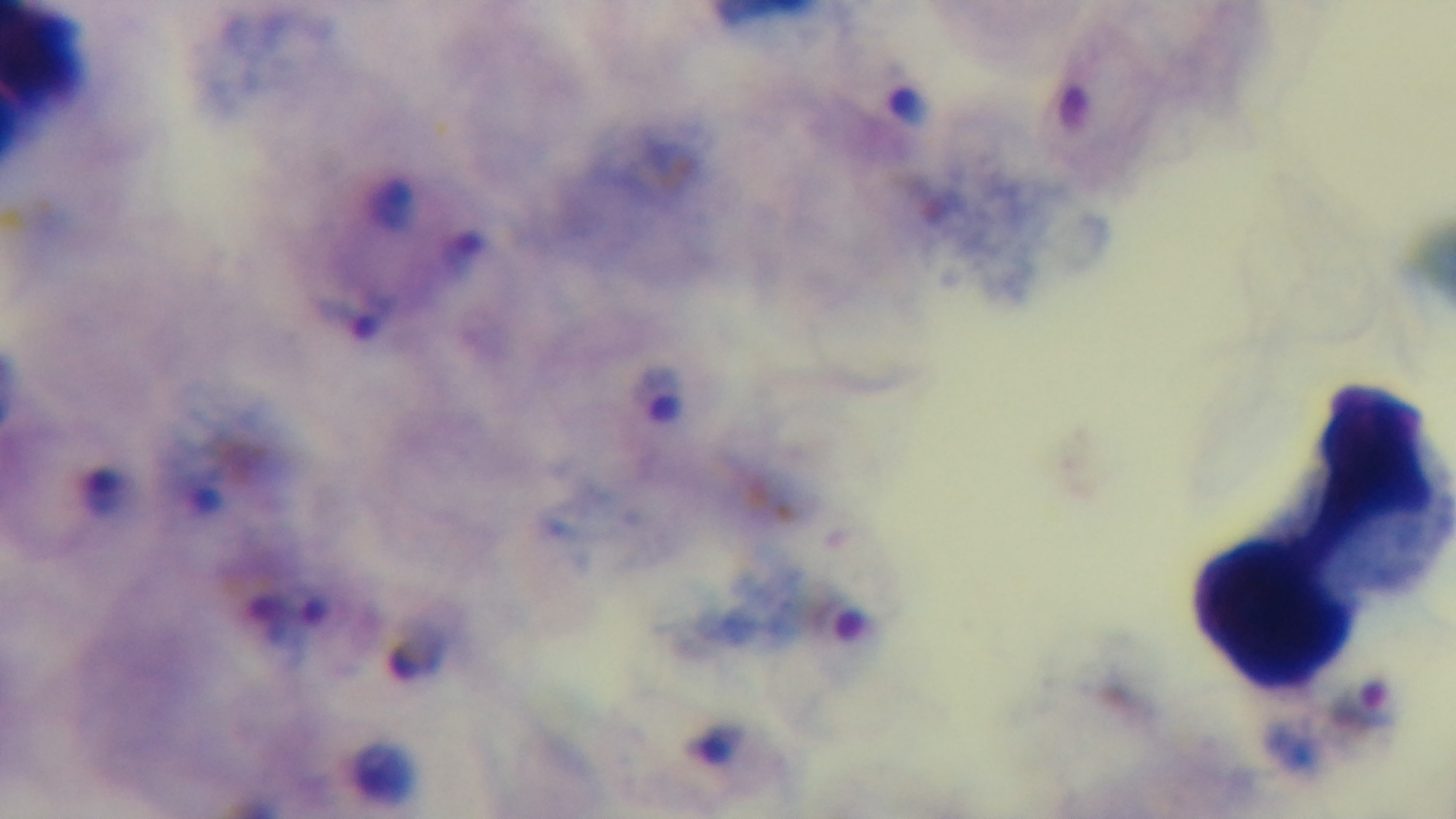

{
  "malaria_status": "infected",
  "capture": "mounted 4K digital camera",
  "preparation": "thick",
  "stain": "Giemsa",
  "objective": "100x oil immersion",
  "field_of_view": "single",
  "modality": "light microscopy"
}